Assess the morphology of the erythrocytes.
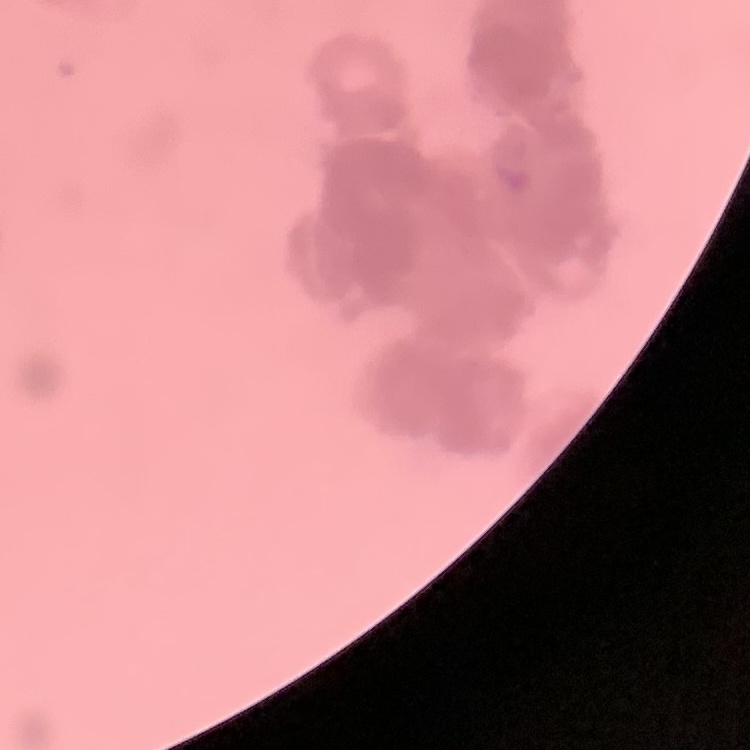
Rouleaux formation.

Thin blood film. One tile cut from a larger photomicrograph. Field's or Giemsa stain.